Assess this cell for malaria.
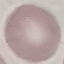
Uninfected.

Cell patch, automatically extracted from a larger field of view and resized to 64 × 64 pixels. Acquired by smartphone through the microscope eyepiece. Giemsa-stained preparation. Thin smear of blood.